Classify this cell by malaria status.
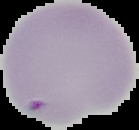

Parasitized.

preparation: thin blood film
image_size: 139×130 pixels
image_type: segmented cell region with the area outside set to black